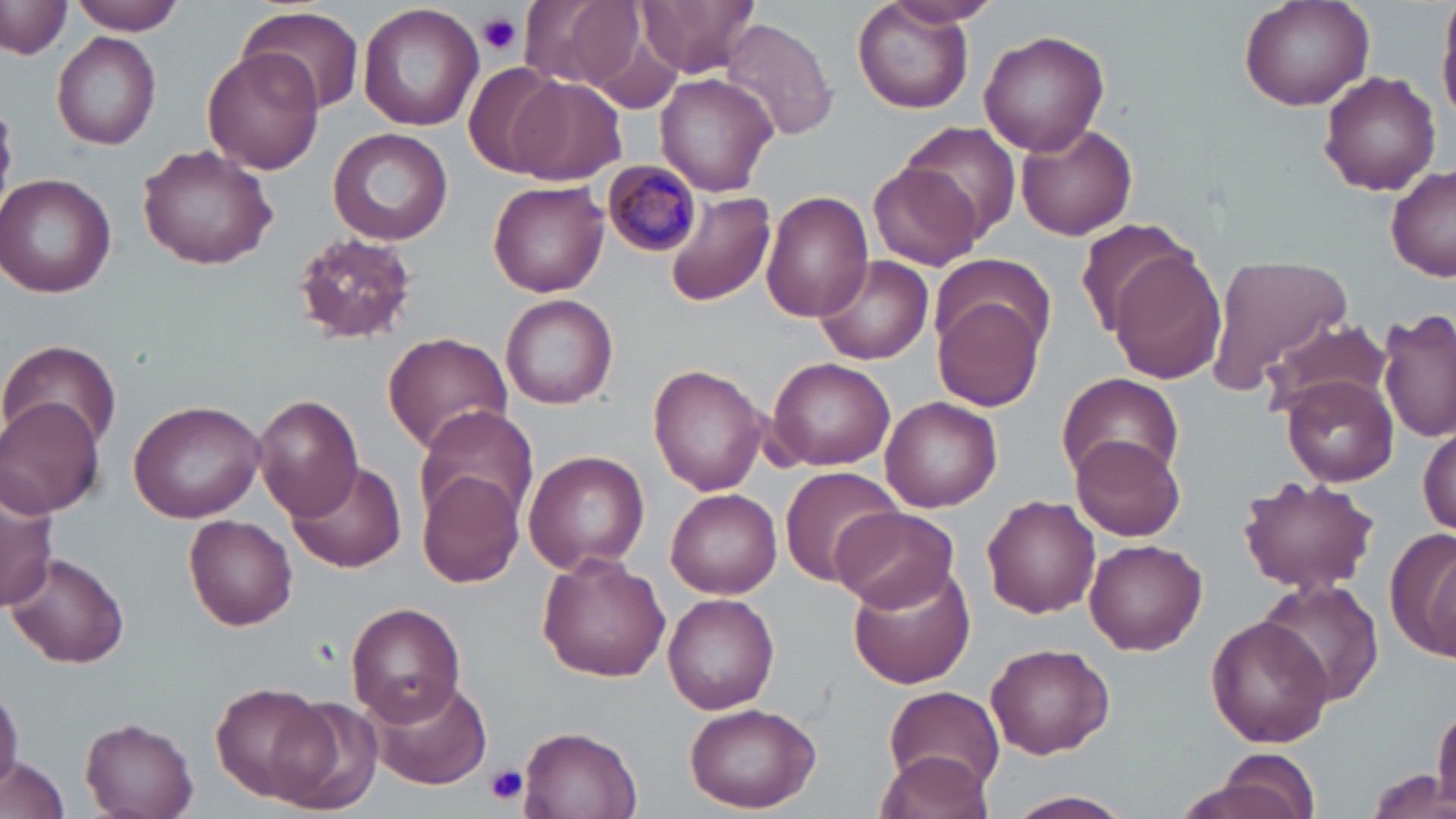
slide-level diagnosis = Plasmodium malariae
platelet locations = approximate bounding boxes as (x1, y1, x2, y2) in pixels: (476, 11, 522, 55), (487, 764, 526, 803)
magnification = 1000x
modality = light microscopy
stain = May-Grünwald-Giemsa
uninfected red blood cell locations = approximate bounding boxes as (x1, y1, x2, y2) in pixels: (64, 0, 188, 35), (517, 0, 638, 90), (638, 0, 760, 76), (851, 0, 976, 114), (1239, 0, 1374, 112), (881, 1, 1000, 30), (1438, 1, 1456, 126), (1, 3, 70, 60), (357, 3, 485, 132), (236, 5, 363, 116), (720, 17, 837, 143), (979, 30, 1110, 155), (51, 31, 162, 149), (202, 48, 326, 176), (463, 64, 566, 177), (1318, 70, 1441, 194), (656, 71, 780, 195), (508, 77, 627, 183), (900, 120, 1019, 240), (1016, 120, 1139, 241), (327, 128, 454, 243), (137, 142, 278, 269), (868, 161, 983, 272), (1386, 167, 1456, 280), (1, 172, 119, 299), (488, 180, 609, 298), (760, 189, 871, 325), (666, 191, 775, 308), (1073, 219, 1201, 338), (290, 231, 418, 345), (1109, 252, 1229, 384), (1206, 252, 1352, 391), (814, 255, 932, 365), (931, 258, 1056, 354), (499, 292, 619, 409), (933, 294, 1044, 412), (1379, 308, 1456, 443), (1265, 321, 1390, 415), (382, 331, 514, 453), (3, 339, 123, 454), (767, 356, 896, 471), (648, 365, 769, 495), (1058, 374, 1184, 486), (1280, 376, 1396, 487), (253, 393, 362, 520), (1, 396, 105, 517), (881, 396, 1002, 511), (127, 398, 266, 522), (414, 405, 542, 526), (1418, 425, 1454, 538), (1070, 432, 1186, 541), (522, 451, 649, 574), (288, 461, 407, 573), (781, 468, 909, 585), (416, 470, 525, 588), (1236, 473, 1381, 597), (1, 484, 60, 610), (667, 489, 781, 599), (983, 495, 1101, 617), (833, 506, 959, 612), (184, 514, 297, 630), (1393, 530, 1455, 663), (1083, 538, 1207, 654), (6, 552, 131, 669), (539, 555, 670, 682), (846, 566, 978, 691), (1254, 578, 1384, 710), (662, 593, 779, 713), (345, 603, 465, 724), (1206, 615, 1333, 747), (985, 643, 1115, 759), (366, 676, 492, 789), (213, 683, 330, 804), (0, 684, 21, 801), (880, 687, 1006, 796), (270, 695, 385, 815), (1432, 701, 1456, 814), (681, 703, 822, 813), (79, 716, 199, 819), (521, 726, 641, 819), (1196, 747, 1324, 819), (874, 748, 997, 816), (0, 757, 71, 819), (1360, 770, 1455, 819), (1003, 790, 1137, 819)
Plasmodium malariae-infected red blood cell locations = approximate bounding boxes as (x1, y1, x2, y2) in pixels: (604, 162, 700, 256)
field of view = one of a larger specimen
image size = 1456×819 pixels
preparation = thin blood film